Locate and identify every blood parasite.
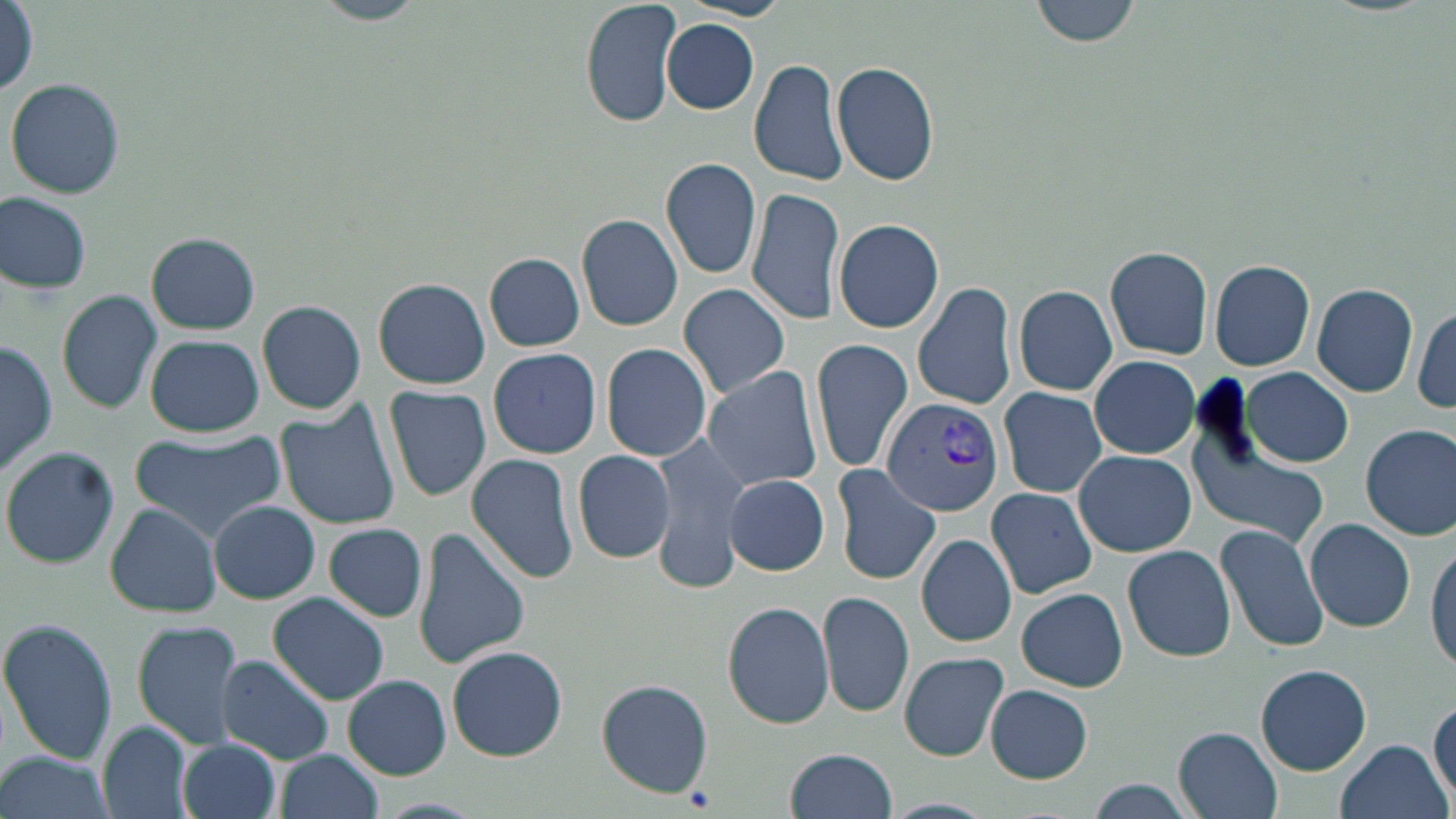

Approximate bounding boxes as (x1,y1)-(x2,y2) corner pairs in pixels.
Plasmodium vivax-infected red blood cells: (882,396)-(1005,516).
No Plasmodium falciparum, Plasmodium ovale, Plasmodium malariae, Babesia divergens, or Trypanosoma brucei observed.

Uninfected red blood cell locations: (309,0)-(430,25), (580,0)-(681,126), (1032,0)-(1140,48), (2,6)-(40,99), (662,20)-(758,114), (748,57)-(848,186), (831,61)-(941,186), (6,78)-(125,200), (660,156)-(762,281), (746,185)-(845,324), (0,193)-(92,293), (577,214)-(684,332), (833,217)-(944,333), (147,233)-(259,334), (1104,246)-(1213,359), (484,254)-(585,352), (1210,258)-(1316,371), (372,278)-(490,389), (913,282)-(1017,410), (677,283)-(792,397), (1013,284)-(1118,395), (1313,284)-(1418,396), (57,289)-(162,413), (1369,297)-(1450,409), (258,299)-(366,415), (1411,305)-(1456,413), (146,334)-(263,436), (1,338)-(59,476), (810,338)-(914,472), (601,343)-(713,463), (488,346)-(601,458), (1089,355)-(1200,458), (701,365)-(826,493), (1243,367)-(1353,467), (385,386)-(492,501), (996,386)-(1107,499), (275,399)-(403,532), (1360,423)-(1456,540), (127,429)-(286,541), (651,433)-(751,592), (1185,433)-(1331,550), (2,447)-(119,570), (573,448)-(676,565), (1073,450)-(1196,557), (465,453)-(579,584), (830,464)-(941,587), (724,474)-(830,576), (986,486)-(1098,600), (208,500)-(321,603), (105,503)-(222,618), (1306,518)-(1415,633), (324,523)-(428,622), (1214,523)-(1331,655), (413,528)-(529,668), (917,533)-(1017,648), (1427,537)-(1456,673), (1122,544)-(1237,661), (1016,587)-(1128,692), (818,590)-(915,719), (269,593)-(389,705), (722,600)-(835,729), (0,619)-(117,767), (133,622)-(245,751), (447,645)-(568,761), (897,652)-(1009,762), (217,654)-(335,764), (1256,663)-(1371,774), (343,675)-(451,779), (595,678)-(714,798), (986,685)-(1093,783), (1428,692)-(1455,810), (99,722)-(194,819), (1174,727)-(1283,819), (178,738)-(281,819), (1336,738)-(1450,819), (785,748)-(898,819), (275,750)-(384,819), (0,751)-(115,819), (1083,778)-(1202,819), (880,799)-(997,819). Slide-level diagnosis: Plasmodium vivax. Thin blood film. Light microscopy. Single field of view. May-Grünwald-Giemsa-stained preparation. Image is 1456×819 pixels. Captured at 1000x magnification.